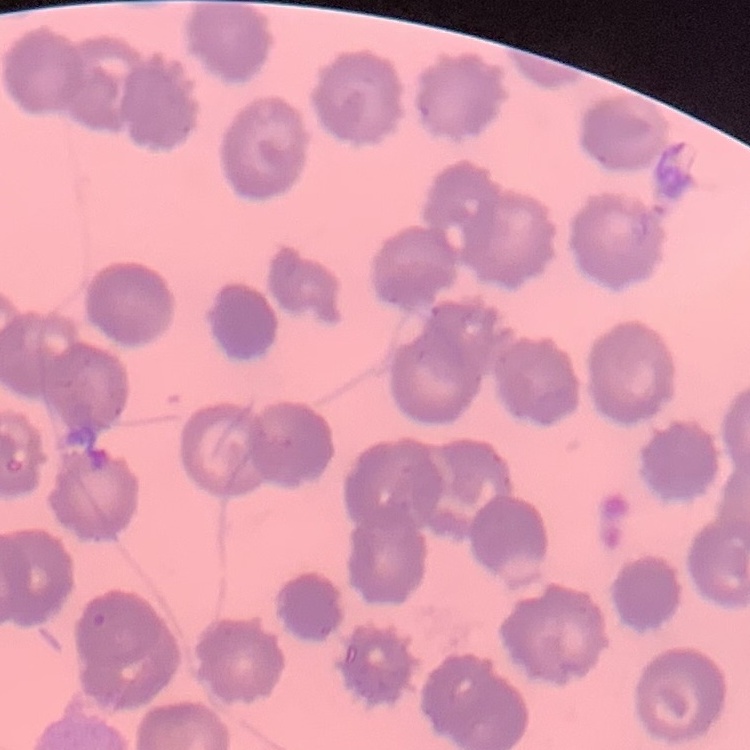 The erythrocytes show no rouleaux formation. Square crop of a larger photomicrograph. Field's or Giemsa stain. Thin blood smear.